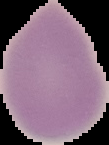

malaria status = uninfected
image size = 109×145 pixels
image type = segmented cell region on a black background
preparation = thin blood film